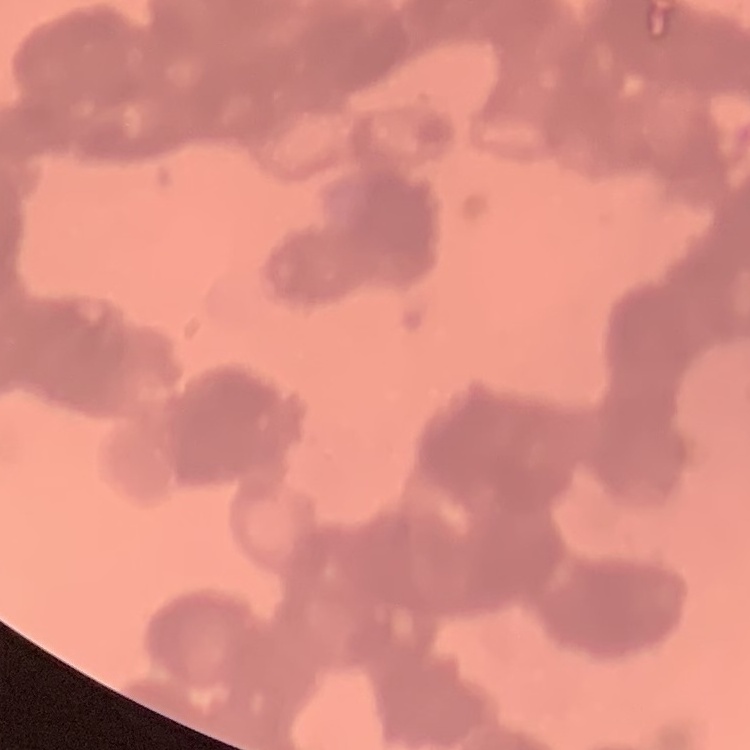
red_blood_cell_morphology: rouleaux formation
stain: Field's or Giemsa
image_type: square crop of a larger photomicrograph
preparation: thin blood smear